Comment on the morphology of the red blood cells.
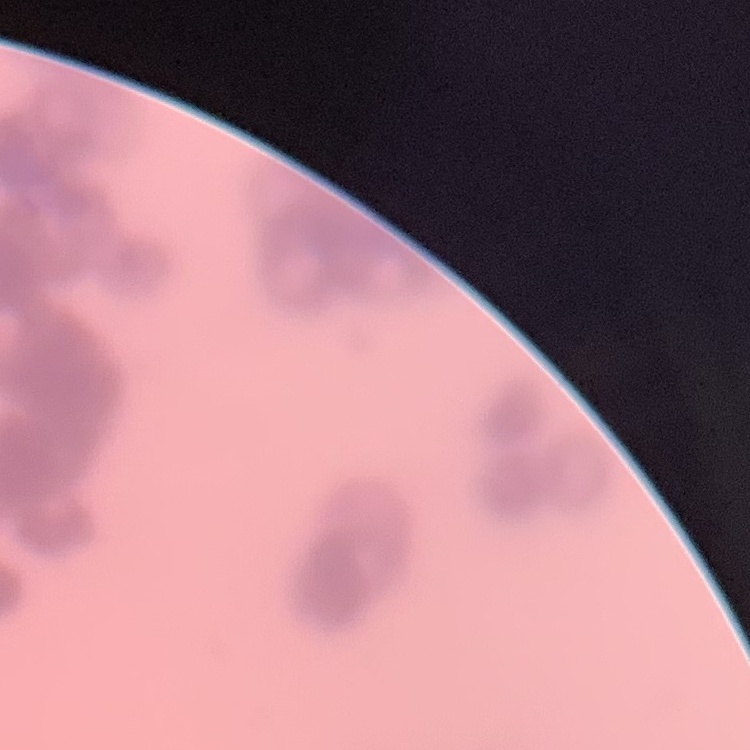
Rouleaux formation.

Summary:
  - Image type: square crop of a larger photomicrograph
  - Preparation: thin blood film
  - Stain: Field's or Giemsa